Describe the morphology of the red blood cells.
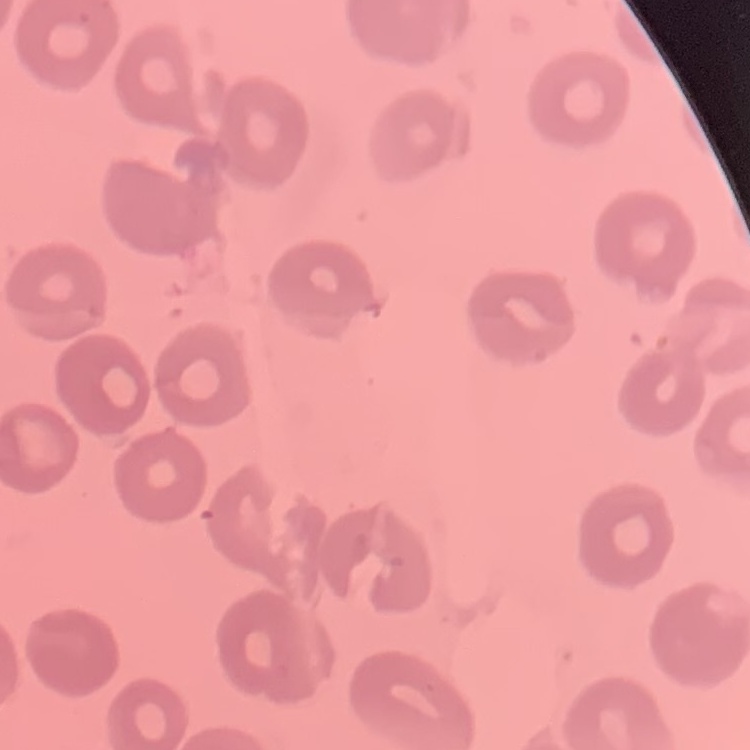
They show no rouleaux formation.

{
  "image_type": "one tile cut from a larger photomicrograph",
  "preparation": "thin blood smear",
  "stain": "Field's or Giemsa"
}